Locate every malaria parasite and every leukocyte.
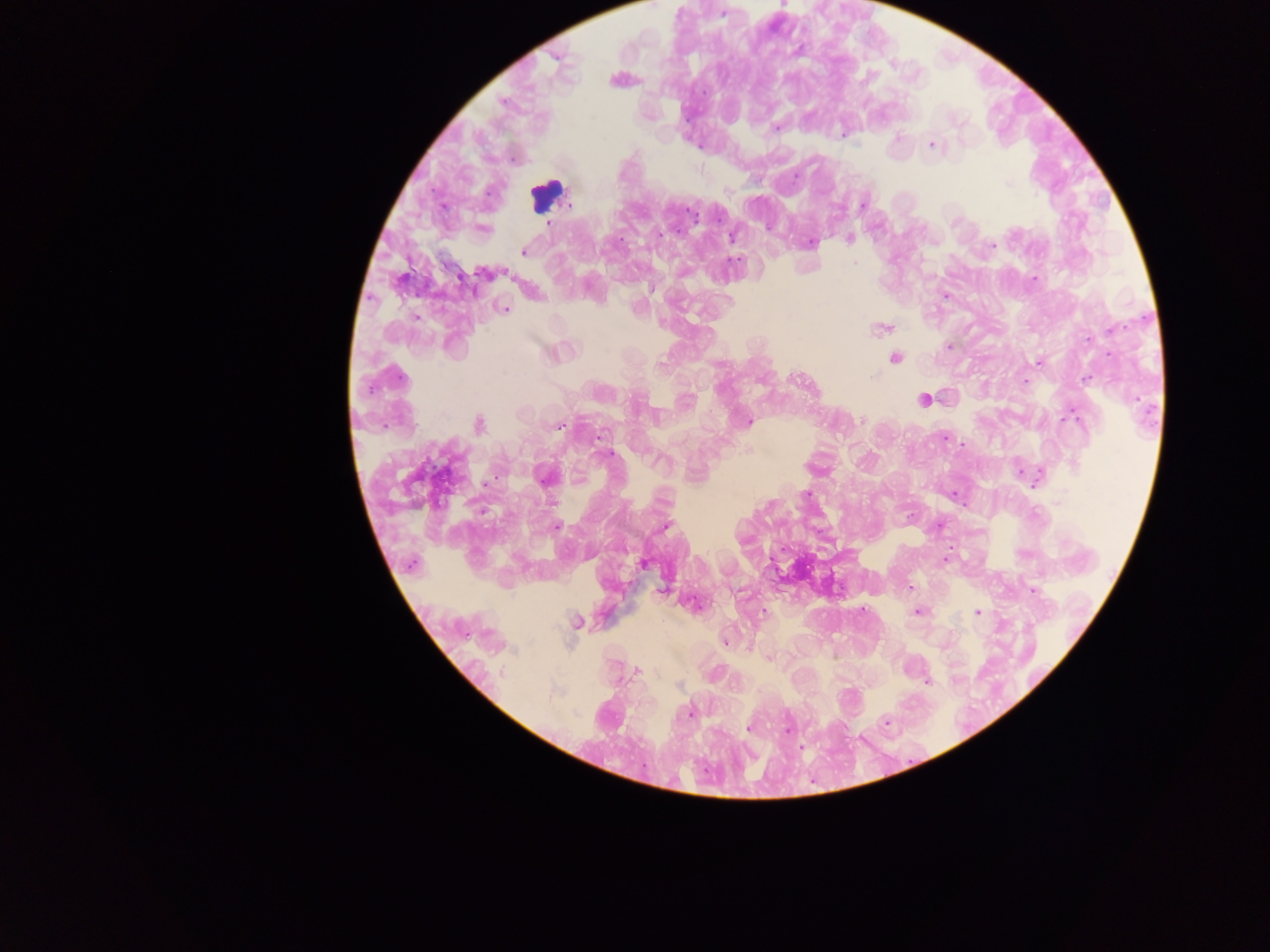
Approximate centers as {x, y} in pixels.
Malaria parasites: {723, 13}, {776, 127}, {932, 145}, {796, 176}, {1009, 183}, {568, 204}, {863, 205}, {549, 223}, {731, 237}, {849, 238}, {810, 243}, {993, 246}, {523, 252}, {855, 263}, {485, 273}, {1033, 279}, {651, 289}, {946, 296}, {505, 309}, {880, 328}, {1111, 329}, {948, 346}, {895, 358}, {1038, 363}, {874, 377}, {1085, 379}, {1025, 381}, {923, 399}, {1071, 417}, {862, 420}, {748, 421}, {479, 424}, {557, 426}, {600, 436}, {945, 438}, {607, 453}, {545, 476}, {806, 493}, {557, 526}, {666, 526}, {945, 559}, {642, 563}, {910, 587}, {662, 591}, {1033, 591}, {918, 612}, {977, 612}, {763, 613}, {576, 622}, {726, 642}, {769, 658}, {637, 670}, {928, 682}, {690, 713}, {886, 723}, {748, 728}, {789, 729}.
Leukocytes: {544, 195}.

Thick blood film. Single field of view. Image is 1270×952 pixels. Sample from Ghana. Photographed through a microscope with a mobile-phone camera.